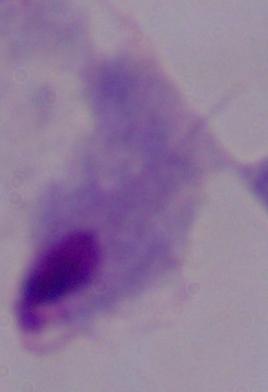
Summary:
  - Magnification: 1000x
  - Identification: trichomonad
  - Modality: micrograph